Assess this cell for malaria.
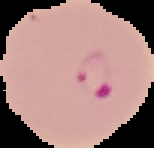

It is parasitized.

Summary:
  - Image type: segmented cell region on a black background
  - Preparation: thin blood smear
  - Image size: 154×148 pixels